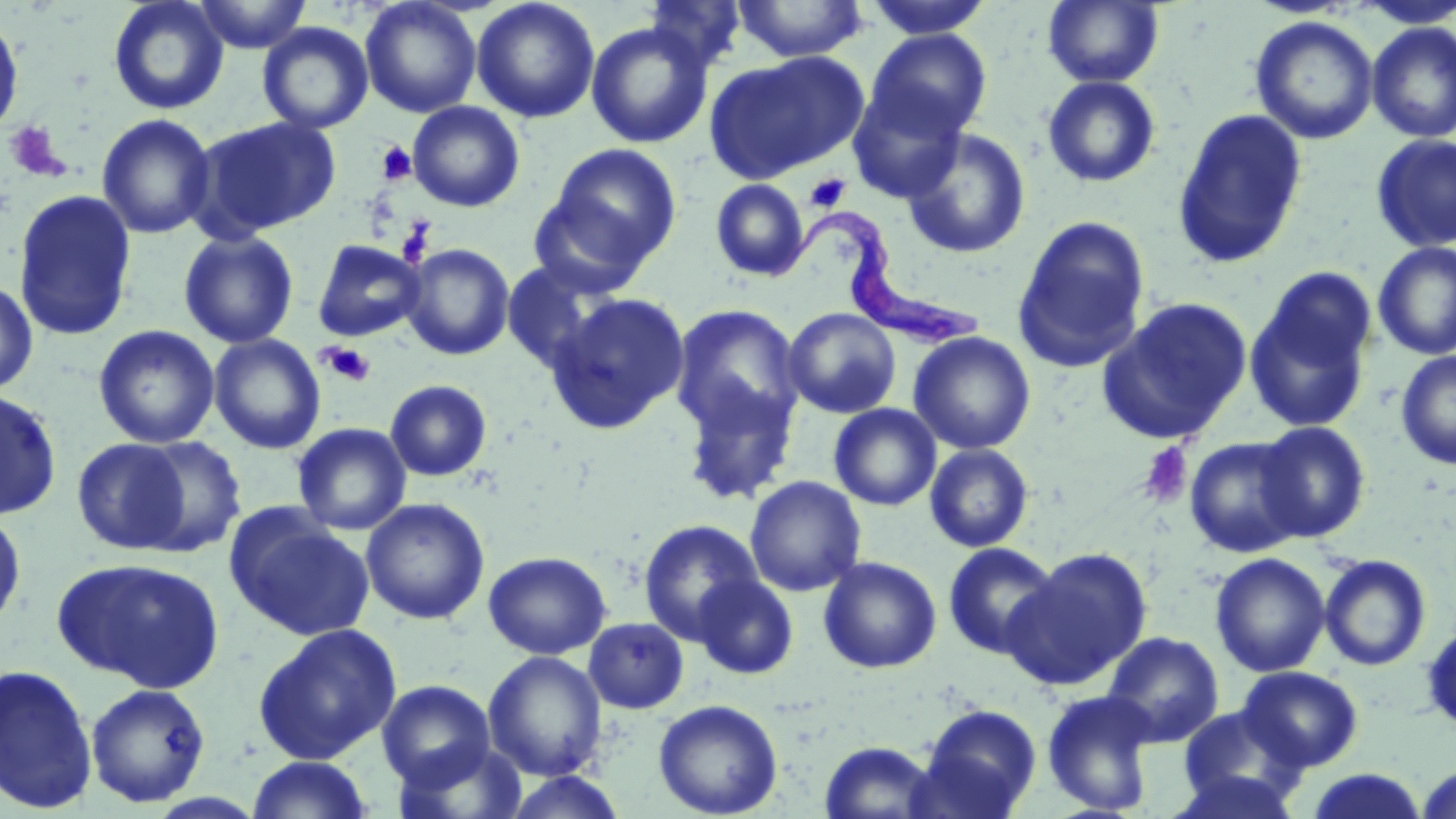
Summary:
  - Coordinate format: approximate bounding boxes as named x1/y1/x2/y2 corners in pixels
  - Platelet locations: (x1=4, y1=121, x2=67, y2=181), (x1=375, y1=141, x2=417, y2=186), (x1=805, y1=173, x2=850, y2=212), (x1=397, y1=219, x2=434, y2=266), (x1=319, y1=342, x2=376, y2=387), (x1=1137, y1=441, x2=1193, y2=508)
  - Uninfected red blood cell locations: (x1=108, y1=0, x2=230, y2=115), (x1=192, y1=0, x2=314, y2=53), (x1=360, y1=0, x2=482, y2=118), (x1=471, y1=0, x2=600, y2=124), (x1=643, y1=0, x2=748, y2=73), (x1=732, y1=0, x2=870, y2=63), (x1=863, y1=0, x2=994, y2=39), (x1=1043, y1=1, x2=1164, y2=88), (x1=1352, y1=1, x2=1456, y2=29), (x1=0, y1=10, x2=25, y2=141), (x1=1250, y1=15, x2=1378, y2=144), (x1=257, y1=21, x2=374, y2=135), (x1=585, y1=21, x2=713, y2=149), (x1=1366, y1=22, x2=1456, y2=142), (x1=866, y1=30, x2=993, y2=141), (x1=704, y1=51, x2=868, y2=184), (x1=1042, y1=76, x2=1162, y2=188), (x1=847, y1=84, x2=968, y2=203), (x1=407, y1=101, x2=525, y2=212), (x1=1172, y1=108, x2=1308, y2=268), (x1=96, y1=113, x2=216, y2=240), (x1=192, y1=115, x2=342, y2=238), (x1=901, y1=128, x2=1031, y2=258), (x1=1371, y1=134, x2=1456, y2=254), (x1=546, y1=143, x2=681, y2=272), (x1=710, y1=179, x2=809, y2=282), (x1=13, y1=189, x2=138, y2=341), (x1=526, y1=193, x2=652, y2=297), (x1=1012, y1=216, x2=1151, y2=372), (x1=179, y1=229, x2=299, y2=348), (x1=312, y1=240, x2=427, y2=341), (x1=1373, y1=242, x2=1456, y2=360), (x1=400, y1=243, x2=516, y2=360), (x1=501, y1=258, x2=620, y2=373), (x1=1243, y1=272, x2=1378, y2=434), (x1=0, y1=279, x2=39, y2=397), (x1=547, y1=292, x2=690, y2=434), (x1=1097, y1=298, x2=1252, y2=445), (x1=669, y1=303, x2=804, y2=438), (x1=782, y1=307, x2=902, y2=418), (x1=93, y1=324, x2=219, y2=448), (x1=908, y1=331, x2=1036, y2=454), (x1=208, y1=333, x2=326, y2=454), (x1=1395, y1=351, x2=1456, y2=469), (x1=677, y1=378, x2=800, y2=504), (x1=385, y1=379, x2=493, y2=482), (x1=0, y1=387, x2=62, y2=519), (x1=829, y1=403, x2=941, y2=511), (x1=1255, y1=421, x2=1372, y2=542), (x1=292, y1=422, x2=411, y2=536), (x1=131, y1=435, x2=247, y2=557), (x1=1183, y1=436, x2=1305, y2=557), (x1=72, y1=437, x2=193, y2=555), (x1=924, y1=443, x2=1034, y2=552), (x1=744, y1=475, x2=867, y2=596), (x1=360, y1=497, x2=490, y2=625), (x1=225, y1=507, x2=376, y2=641), (x1=0, y1=509, x2=26, y2=633), (x1=638, y1=520, x2=763, y2=644), (x1=943, y1=542, x2=1062, y2=661), (x1=1005, y1=547, x2=1153, y2=691), (x1=483, y1=550, x2=611, y2=659), (x1=1210, y1=552, x2=1331, y2=677), (x1=1319, y1=554, x2=1432, y2=671), (x1=52, y1=556, x2=227, y2=692), (x1=818, y1=556, x2=942, y2=673), (x1=693, y1=574, x2=798, y2=680), (x1=583, y1=617, x2=690, y2=713), (x1=1421, y1=621, x2=1456, y2=736), (x1=252, y1=623, x2=403, y2=765), (x1=1102, y1=631, x2=1224, y2=747), (x1=483, y1=651, x2=607, y2=781), (x1=0, y1=663, x2=98, y2=814), (x1=1238, y1=666, x2=1363, y2=771), (x1=377, y1=680, x2=496, y2=787), (x1=85, y1=683, x2=211, y2=807), (x1=1041, y1=689, x2=1159, y2=816), (x1=653, y1=698, x2=783, y2=818), (x1=914, y1=704, x2=1041, y2=818), (x1=1176, y1=705, x2=1306, y2=811), (x1=390, y1=739, x2=529, y2=819), (x1=819, y1=740, x2=939, y2=818), (x1=247, y1=755, x2=373, y2=818), (x1=1416, y1=764, x2=1456, y2=819), (x1=1304, y1=768, x2=1429, y2=818), (x1=1167, y1=769, x2=1302, y2=818), (x1=501, y1=770, x2=629, y2=818)
  - Trypanosoma brucei locations: (x1=765, y1=211, x2=987, y2=352)
  - Slide-level diagnosis: Trypanosoma brucei
  - Preparation: thin blood smear
  - Modality: light microscopy
  - Magnification: 1000x
  - Image size: 1456×819 pixels
  - Stain: May-Grünwald-Giemsa
  - Field of view: one of a larger specimen